Describe the morphology of the red blood cells.
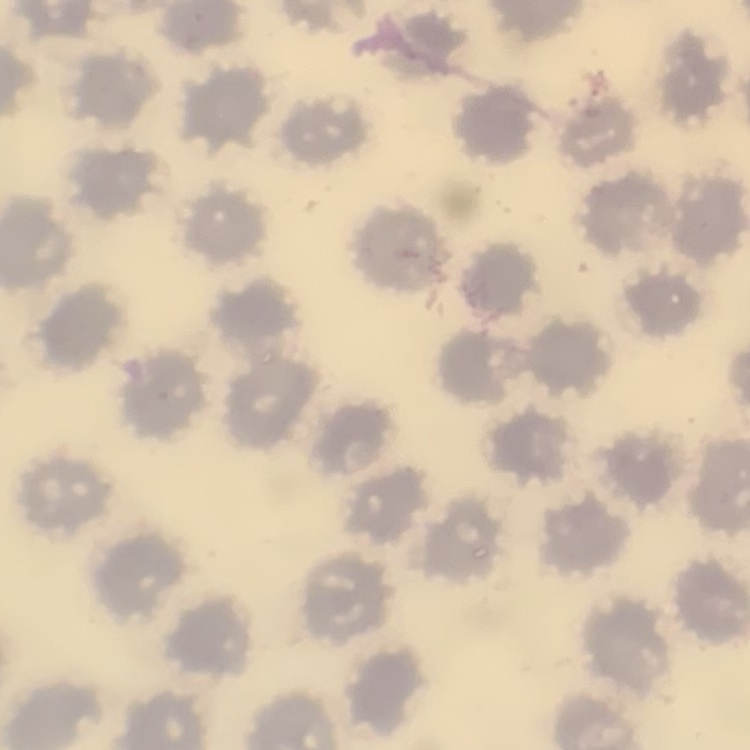
They show no rouleaux formation.

preparation = thin blood smear
image type = square crop of a larger photomicrograph
stain = Field's or Giemsa